Outline each uninfected red blood cell.
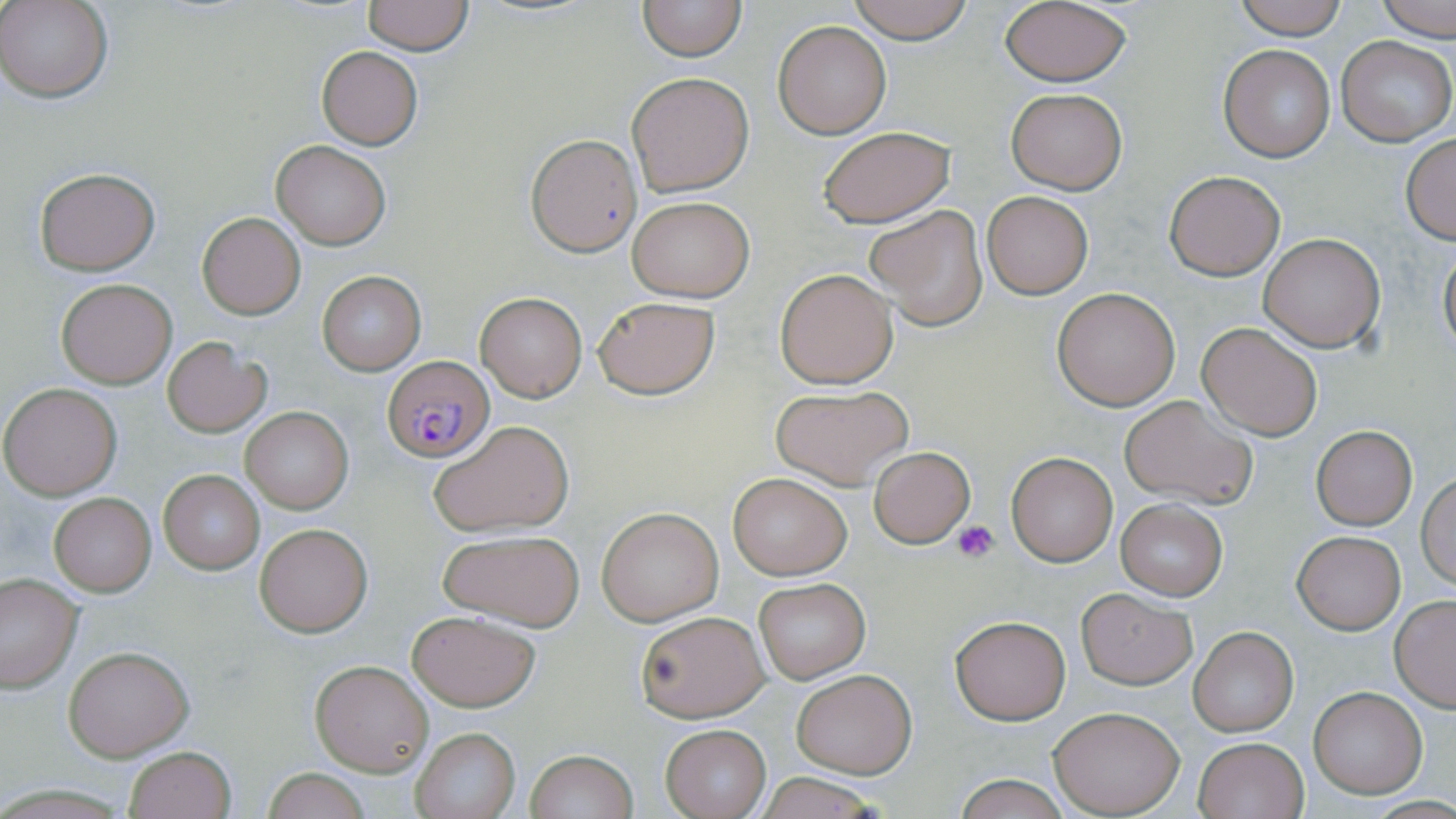
Approximate bounding boxes as (x1, y1, x2, y2) in pixels.
Uninfected red blood cells: (2, 0, 112, 102), (361, 0, 474, 54), (636, 0, 747, 61), (844, 0, 977, 42), (1231, 0, 1348, 40), (1378, 0, 1456, 42), (998, 2, 1132, 86), (772, 20, 891, 139), (1335, 36, 1454, 148), (1219, 44, 1334, 162), (316, 46, 423, 150), (627, 72, 754, 196), (1006, 88, 1126, 193), (817, 127, 955, 228), (525, 133, 642, 257), (1401, 134, 1456, 243), (271, 139, 391, 250), (33, 168, 160, 275), (1163, 171, 1285, 280), (982, 191, 1093, 299), (627, 197, 753, 303), (864, 204, 989, 331), (196, 211, 306, 320), (1258, 233, 1385, 353), (1438, 243, 1456, 361), (775, 268, 899, 389), (317, 271, 424, 375), (56, 278, 177, 388), (1051, 287, 1182, 411), (475, 291, 586, 401), (591, 295, 720, 400), (1196, 321, 1324, 440), (163, 338, 271, 438), (0, 383, 123, 500), (770, 384, 913, 490), (1119, 395, 1257, 509), (240, 404, 354, 515), (428, 422, 576, 537), (1311, 426, 1417, 529), (868, 447, 974, 548), (1004, 451, 1119, 567), (158, 471, 264, 573), (1417, 471, 1456, 589), (727, 473, 851, 579), (49, 492, 156, 597), (1115, 498, 1227, 599), (596, 506, 724, 626), (254, 522, 373, 637), (438, 528, 585, 630), (1292, 530, 1405, 635), (0, 574, 83, 693), (753, 578, 870, 683), (1074, 587, 1198, 691), (1390, 594, 1456, 710), (406, 610, 539, 712), (634, 610, 769, 722), (950, 612, 1072, 725), (1187, 627, 1298, 736), (65, 644, 194, 761), (309, 659, 433, 777), (791, 668, 916, 778), (1309, 687, 1427, 798), (1048, 706, 1185, 815), (660, 724, 770, 817), (410, 728, 519, 818), (1193, 736, 1309, 819), (123, 746, 236, 819), (523, 750, 638, 819), (259, 767, 374, 819), (754, 772, 886, 818), (952, 775, 1071, 818).

Summary:
  - Plasmodium falciparum-infected red blood cell locations: (385, 354, 496, 464)
  - Platelet locations: (951, 521, 1001, 564)
  - Slide-level diagnosis: Plasmodium falciparum
  - Field of view: one of a larger specimen
  - Magnification: 1000x
  - Modality: optical microscopy
  - Stain: May-Grünwald-Giemsa
  - Preparation: thin blood smear
  - Image size: 1456×819 pixels